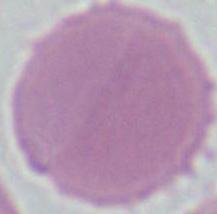
Photomicrograph. An erythrocyte is seen. Captured at 1000x magnification.